Look for Plasmodium parasites.
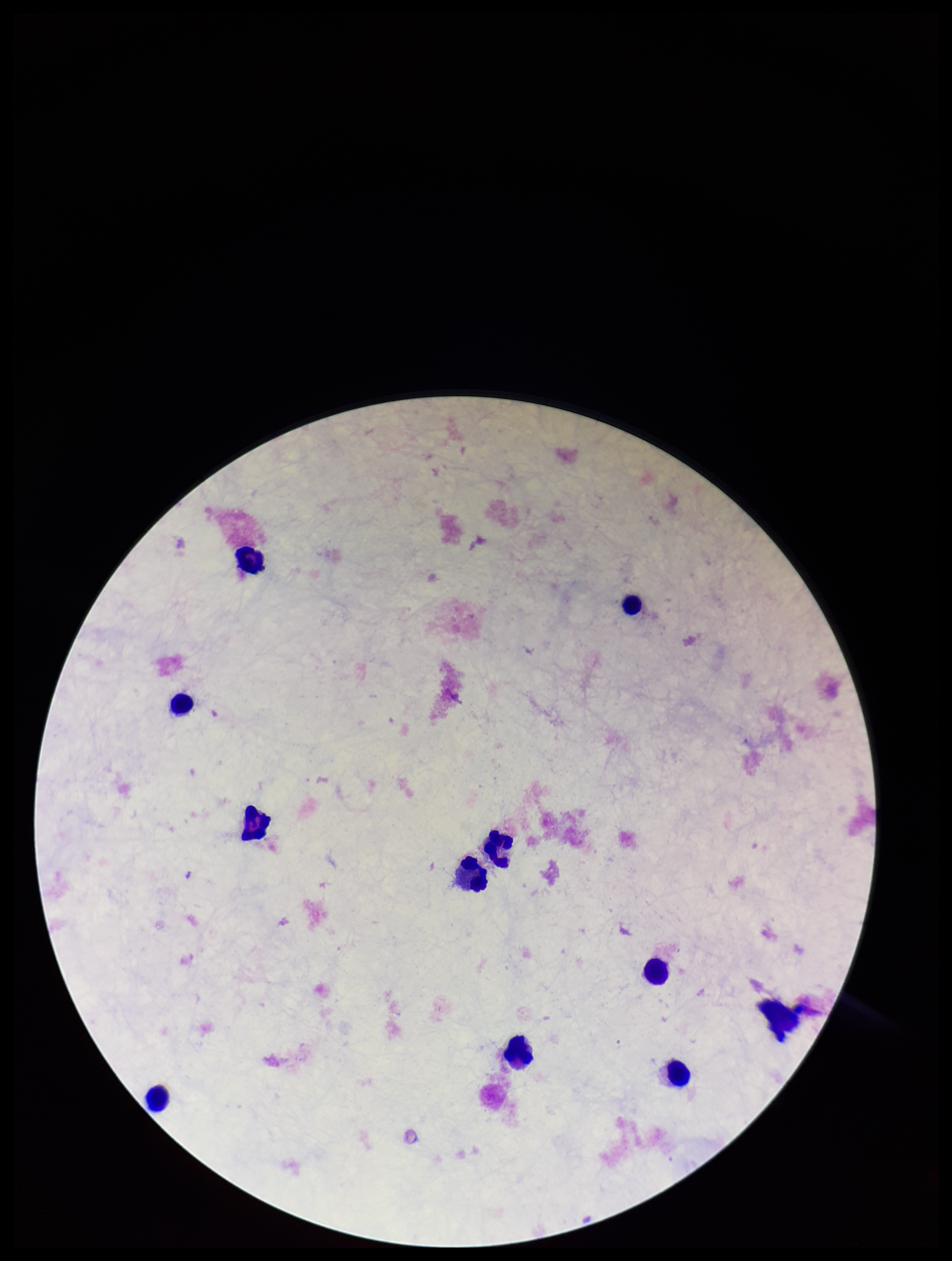
None seen.

Image is 952×1261 pixels. One field from this slide. Preparation: thick blood smear. Parasite count: 0. Patient malaria status: negative. Smartphone photograph taken through the eyepiece of a microscope. Giemsa stain. Leukocyte count: 10.